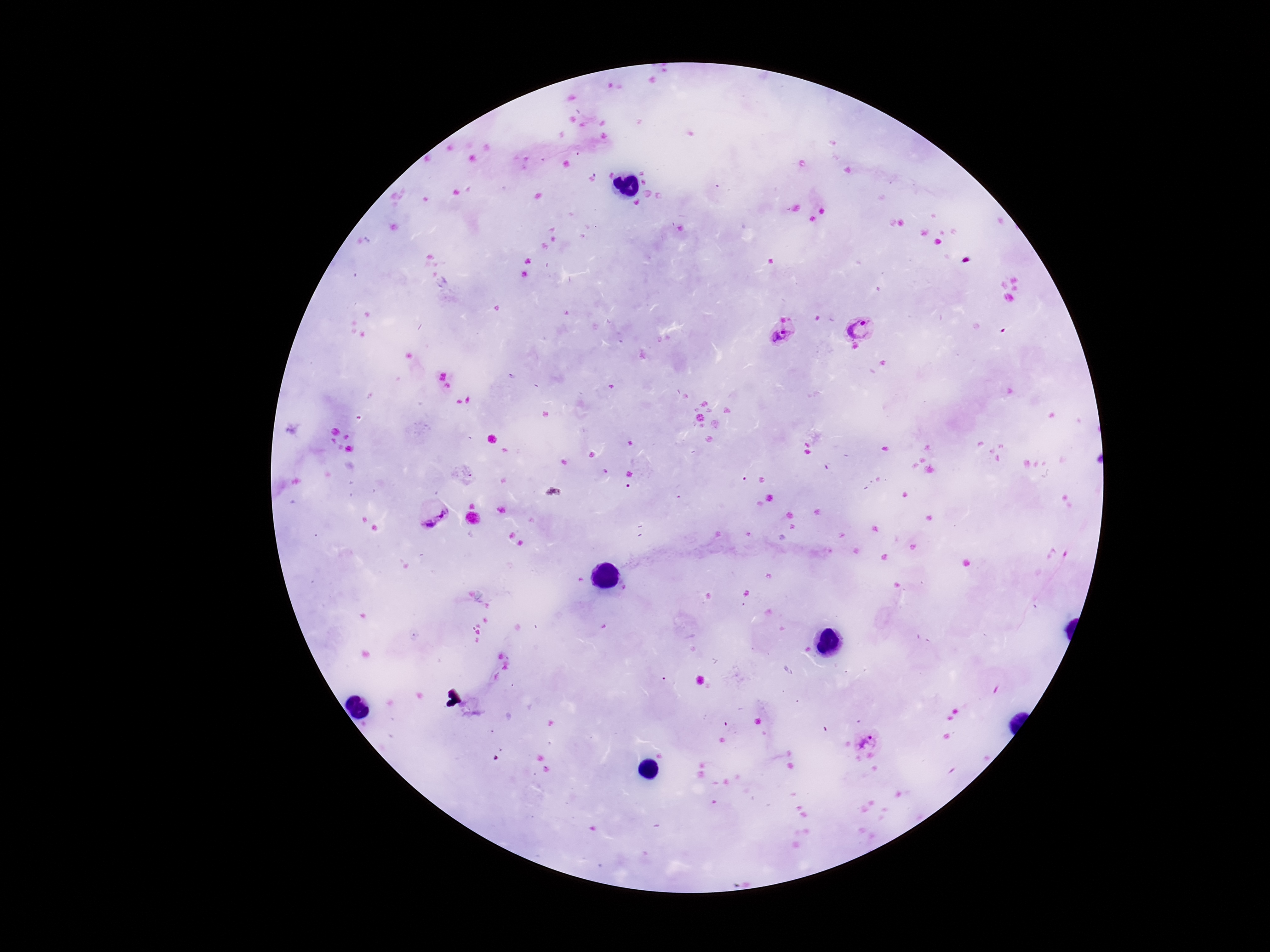
Approximate centers as {x, y} in pixels.
Summary:
  - Plasmodium parasite locations: {863, 327}, {783, 337}, {434, 521}, {866, 739}
  - Image size: 1270×952 pixels
  - Stain: Giemsa
  - Field of view: single
  - Magnification: 100x
  - Patient malaria status: infected
  - Capture: smartphone camera through the microscope eyepiece
  - Preparation: thick peripheral-blood smear